Report the malaria status of this cell.
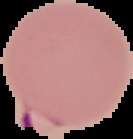
Parasitized.

image type = segmented cell region on a black background
image size = 133×139 pixels
preparation = thin blood smear